Assess this cell for malaria.
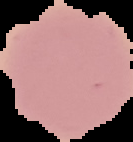

It is uninfected.

image_type: cell region segmented out of the field of view; surrounding area masked to black
preparation: thin blood film
image_size: 133×142 pixels